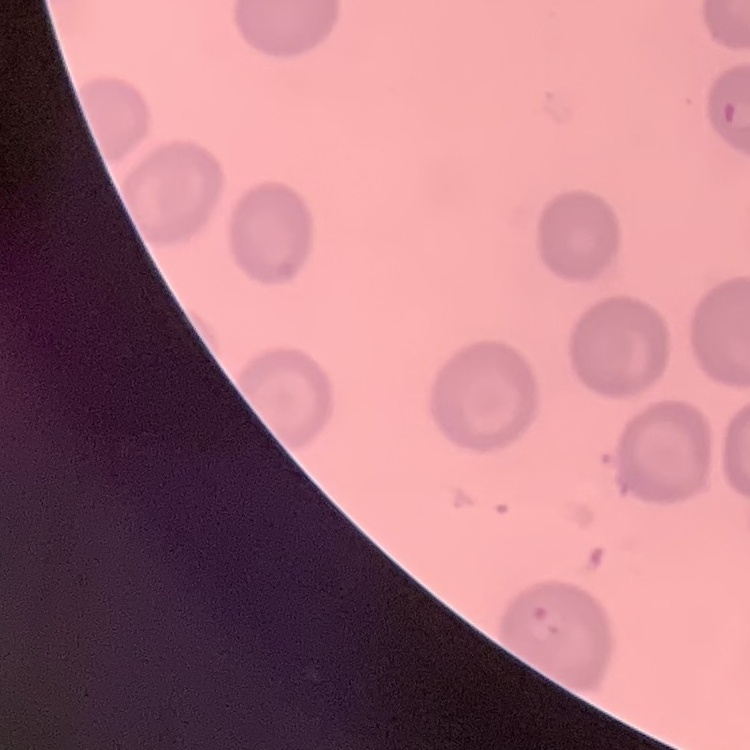
The erythrocytes show no rouleaux formation. Thin blood smear. Stained with either Field's or Giemsa. Square crop of a larger photomicrograph.